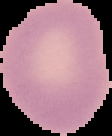

Summary:
  - Image type: segmented cell region on a black background
  - Result: no Plasmodium parasites seen
  - Image size: 112×136 pixels
  - Preparation: thin blood smear